State which parasite is depicted.
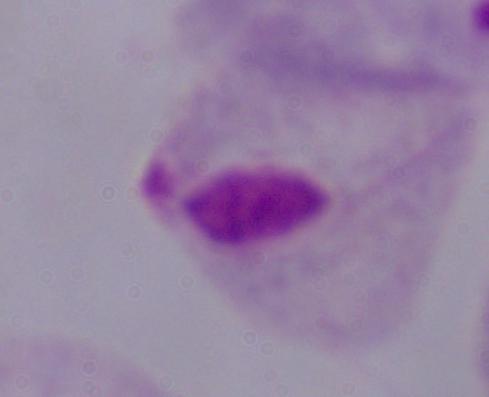

A trichomonad.

Summary:
  - Magnification: 1000x
  - Modality: photomicrograph